Classify this cell by malaria status.
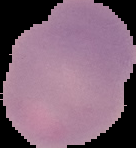
Uninfected.

Segmented cell region on a black background. From a thin blood film. Image is 136×148 pixels.